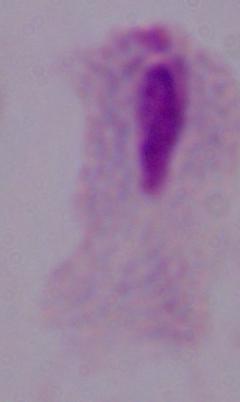
Summary:
  - Identification: trichomonad
  - Modality: micrograph
  - Magnification: 1000x